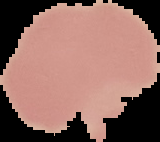 From a thin blood smear. Result: negative for Plasmodium parasites. The area outside the segmented cell region is set to black. Image is 160×142 pixels.